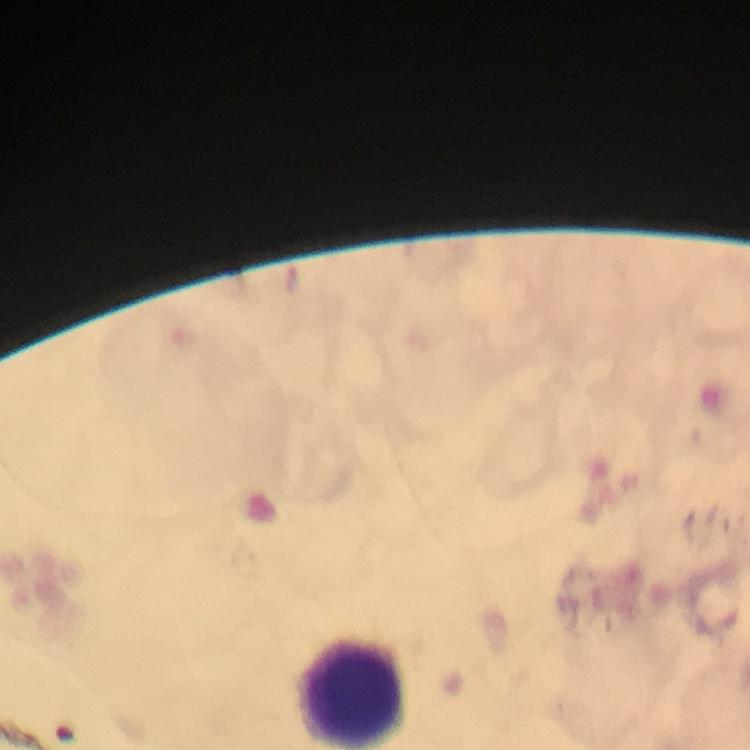

Approximate centers as {x, y} in pixels.
Summary:
  - Leukocyte locations: {350, 694}
  - Capture: smartphone photograph through a microscope
  - Stain: Giemsa
  - Context: from a diagnostic examination for malaria
  - Magnification: 100x
  - Immersion oil: applied
  - Preparation: thick blood smear
  - Image size: 750×750 pixels
  - Cropped from: a single field of view
  - Plasmodium parasites: none seen